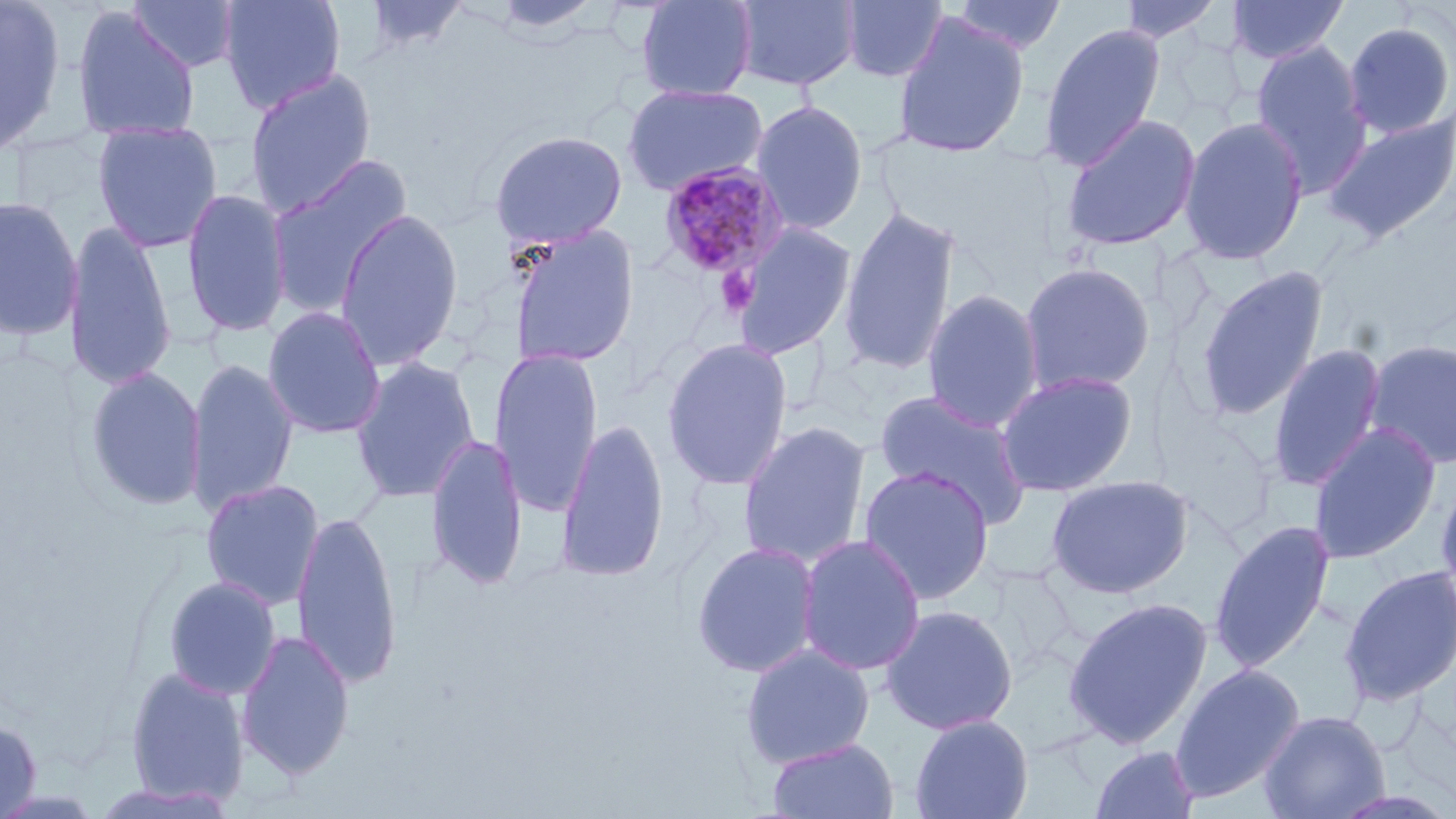

Approximate bounding boxes as (x1,y1)-(x2,y2) corner pairs in pixels. Platelet locations: (715,267)-(761,317). Plasmodium malariae-infected red blood cell locations: (656,162)-(791,280). Uninfected red blood cell locations: (0,0)-(67,159), (218,0)-(346,115), (361,0)-(472,55), (488,0)-(604,38), (636,0)-(758,101), (731,0)-(861,91), (839,0)-(948,84), (946,0)-(1069,57), (1118,0)-(1224,43), (1225,0)-(1350,64), (127,1)-(243,75), (70,7)-(201,143), (892,13)-(1029,159), (1342,21)-(1456,140), (1039,22)-(1166,171), (1164,32)-(1249,122), (1251,39)-(1372,195), (244,68)-(377,217), (621,83)-(768,195), (751,100)-(868,234), (1060,113)-(1201,252), (1322,113)-(1456,244), (1179,117)-(1308,266), (92,120)-(223,253), (488,129)-(627,249), (266,154)-(414,320), (181,188)-(291,337), (0,195)-(84,341), (836,203)-(962,376), (334,208)-(464,371), (730,221)-(858,359), (63,222)-(178,391), (507,224)-(641,369), (1019,261)-(1157,396), (1195,266)-(1329,421), (921,288)-(1045,432), (262,306)-(386,439), (661,337)-(794,492), (1363,338)-(1456,470), (1267,342)-(1387,493), (489,346)-(604,518), (350,356)-(480,503), (185,357)-(299,517), (84,366)-(207,511), (996,371)-(1138,497), (874,390)-(1031,527), (555,418)-(671,582), (737,421)-(872,569), (1308,422)-(1442,565), (426,433)-(529,591), (858,465)-(995,605), (1435,471)-(1456,613), (1045,474)-(1195,598), (200,479)-(324,611), (292,510)-(402,689), (1209,520)-(1336,673), (796,535)-(926,675), (691,540)-(821,678), (1339,565)-(1456,706), (162,576)-(282,701), (1062,597)-(1213,750), (880,604)-(1018,735), (235,629)-(356,780), (740,643)-(875,769), (1170,664)-(1305,802), (123,667)-(250,808), (1259,709)-(1391,819), (909,714)-(1034,819), (0,717)-(42,819), (767,737)-(900,819), (1090,744)-(1201,819), (91,781)-(237,817). Slide-level diagnosis: Plasmodium malariae. One field of a larger specimen. Image is 1456×819 pixels. Thin blood film. May-Grünwald-Giemsa stain. 1000x magnification. Light microscopy.